Report the malaria status of this cell.
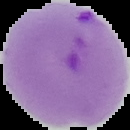

Parasitized.

{
  "preparation": "thin blood film",
  "image_type": "segmented cell region with the area outside set to black",
  "image_size": "130×130 pixels"
}